Name the cell type shown.
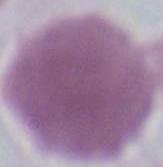

This is an erythrocyte.

Summary:
  - Modality: photomicrograph
  - Magnification: 1000x